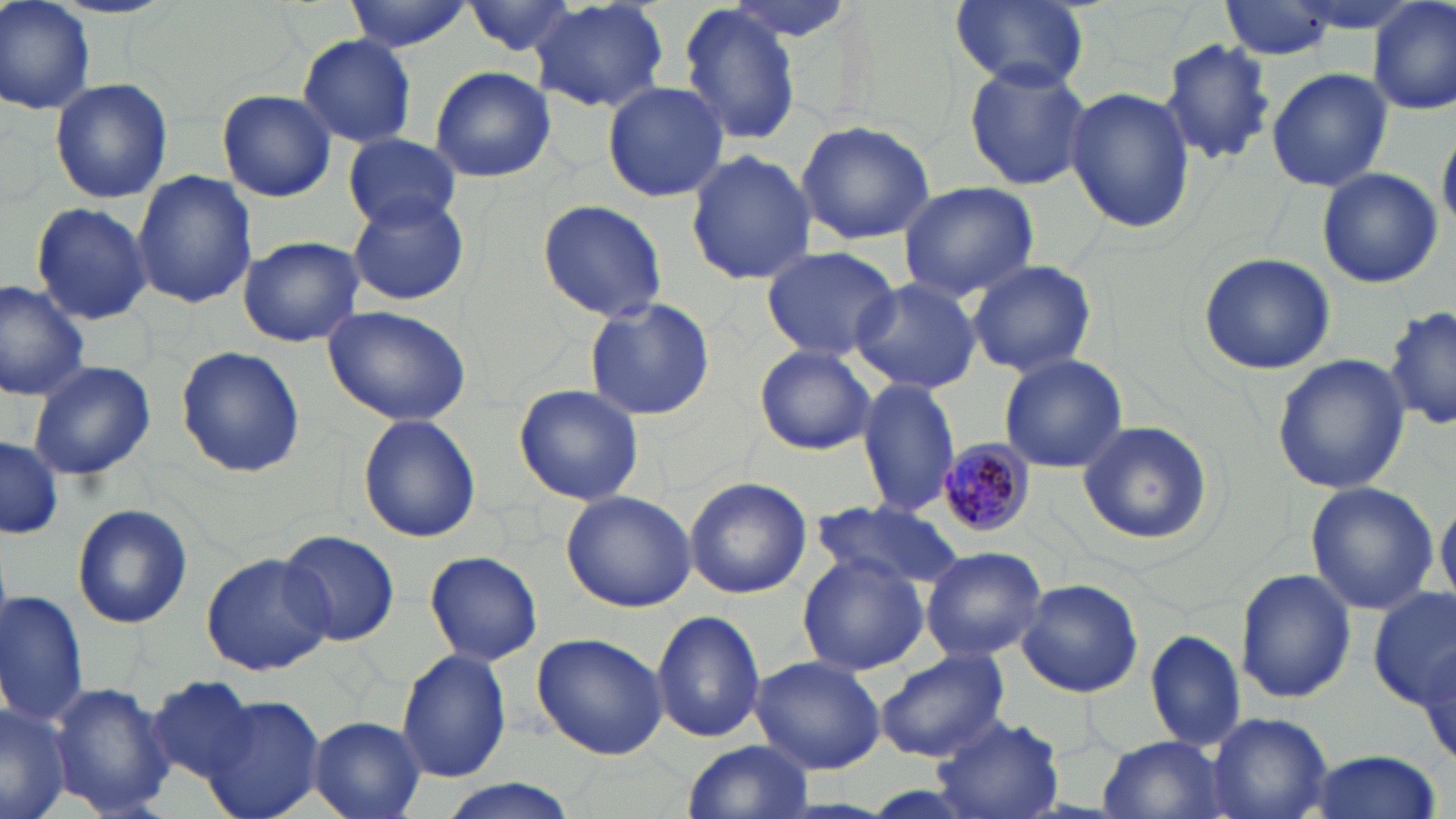
Approximate bounding boxes as (x1,y1)-(x2,y2) corner pairs in pixels. Uninfected red blood cell locations: (1,0)-(96,114), (343,0)-(475,51), (529,0)-(668,113), (717,0)-(858,45), (948,0)-(1093,94), (462,1)-(587,58), (1219,1)-(1342,60), (1369,1)-(1456,116), (676,4)-(804,145), (297,34)-(417,146), (1161,37)-(1276,166), (962,62)-(1093,192), (429,65)-(556,183), (1265,66)-(1393,193), (50,78)-(173,205), (601,80)-(730,203), (1065,86)-(1195,234), (216,89)-(337,202), (795,119)-(936,246), (1438,122)-(1456,233), (342,132)-(461,232), (685,149)-(816,287), (1316,168)-(1445,288), (133,171)-(257,307), (899,181)-(1038,300), (344,192)-(471,308), (537,199)-(667,321), (31,202)-(153,325), (237,235)-(365,348), (760,244)-(901,362), (1198,251)-(1336,375), (967,260)-(1097,378), (851,279)-(984,394), (0,280)-(91,401), (584,296)-(715,422), (319,305)-(474,428), (1387,305)-(1454,434), (176,345)-(305,477), (754,345)-(879,455), (1271,350)-(1409,495), (998,354)-(1129,474), (27,358)-(155,482), (1019,373)-(1170,506), (857,378)-(962,520), (512,383)-(644,505), (357,413)-(482,543), (1077,421)-(1213,545), (1,436)-(62,540), (685,477)-(811,600), (1302,480)-(1438,615), (560,490)-(697,611), (1436,493)-(1455,606), (810,500)-(965,588), (73,503)-(192,629), (279,530)-(400,646), (919,545)-(1047,662), (425,550)-(545,666), (199,552)-(333,676), (796,552)-(928,675), (1235,568)-(1357,706), (1017,578)-(1144,698), (1371,587)-(1456,714), (0,589)-(89,730), (652,610)-(766,743), (1144,628)-(1246,753), (531,632)-(669,759), (1413,640)-(1453,770), (397,647)-(513,784), (873,650)-(1012,764), (750,655)-(884,774), (148,676)-(258,780), (44,680)-(174,816), (203,696)-(326,819), (0,699)-(77,819), (932,712)-(1066,818), (1206,713)-(1334,819), (308,716)-(425,818), (1097,735)-(1233,819), (683,741)-(816,818), (1304,750)-(1445,819), (428,781)-(581,819). Plasmodium malariae-infected red blood cell locations: (933,440)-(1036,538). Slide-level diagnosis: Plasmodium malariae. 1000x magnification. Optical microscopy. May-Grünwald-Giemsa-stained preparation. Image is 1456×819 pixels. Thin blood smear. One field of a larger specimen.